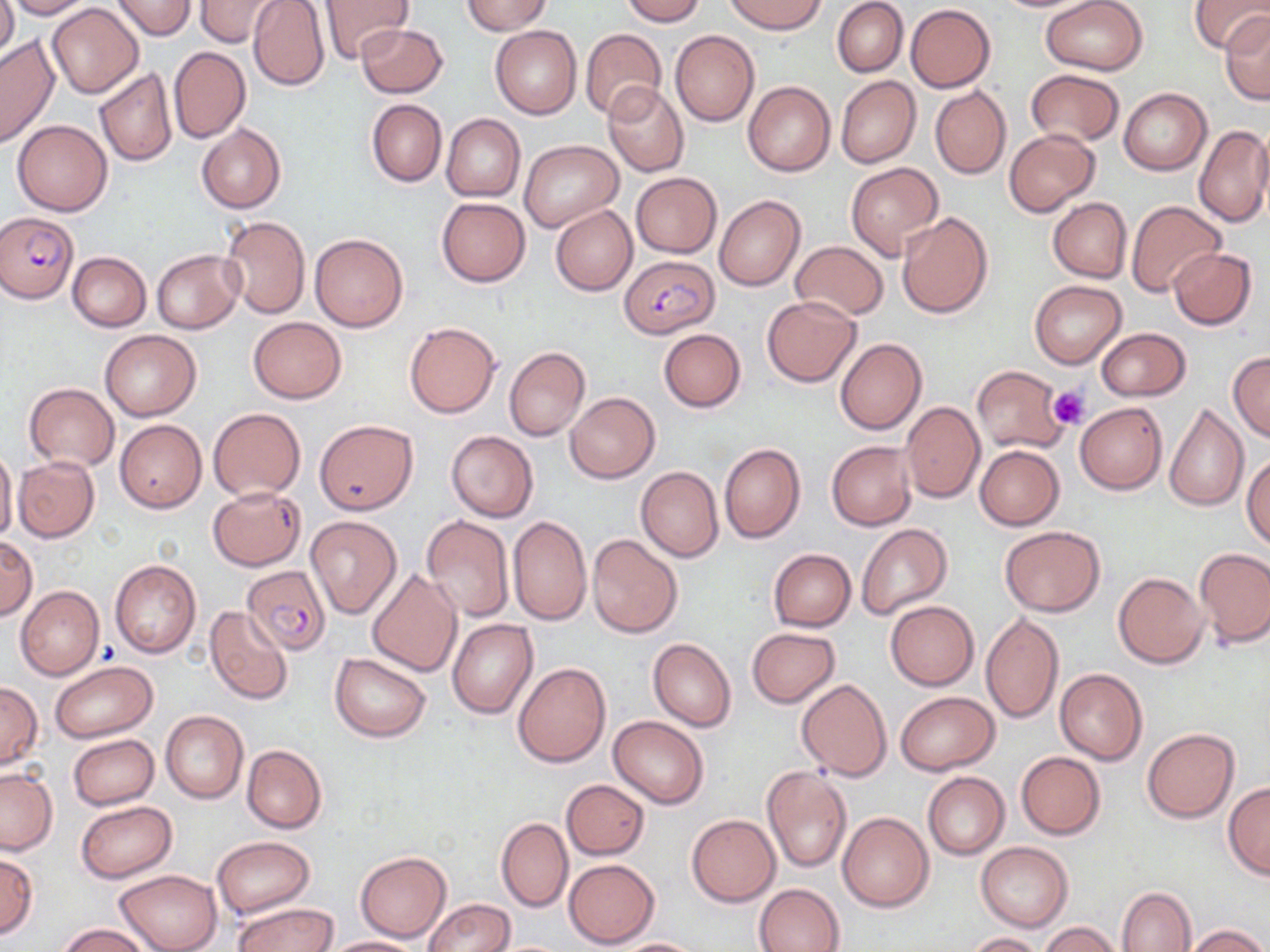

Summary:
  - Coordinate format: approximate bounding boxes as named x1/y1/x2/y2 corners in pixels
  - Plasmodium falciparum-infected red blood cell locations: (x1=0, y1=214, x2=78, y2=303), (x1=619, y1=255, x2=718, y2=338), (x1=242, y1=564, x2=331, y2=655)
  - Platelet locations: (x1=1048, y1=386, x2=1090, y2=430)
  - Uninfected red blood cell locations: (x1=0, y1=0, x2=17, y2=64), (x1=5, y1=0, x2=95, y2=19), (x1=111, y1=0, x2=196, y2=40), (x1=195, y1=0, x2=284, y2=48), (x1=317, y1=0, x2=413, y2=63), (x1=465, y1=0, x2=550, y2=35), (x1=620, y1=0, x2=705, y2=25), (x1=724, y1=0, x2=826, y2=34), (x1=832, y1=0, x2=908, y2=77), (x1=1042, y1=0, x2=1147, y2=75), (x1=1189, y1=0, x2=1268, y2=53), (x1=249, y1=1, x2=331, y2=92), (x1=46, y1=3, x2=144, y2=98), (x1=906, y1=4, x2=996, y2=92), (x1=1219, y1=12, x2=1270, y2=105), (x1=356, y1=23, x2=448, y2=98), (x1=490, y1=25, x2=582, y2=119), (x1=580, y1=28, x2=666, y2=121), (x1=670, y1=30, x2=759, y2=126), (x1=0, y1=34, x2=59, y2=147), (x1=170, y1=46, x2=250, y2=143), (x1=94, y1=69, x2=178, y2=166), (x1=1027, y1=69, x2=1123, y2=146), (x1=835, y1=76, x2=921, y2=169), (x1=743, y1=81, x2=835, y2=177), (x1=603, y1=83, x2=689, y2=176), (x1=930, y1=85, x2=1011, y2=179), (x1=1120, y1=87, x2=1212, y2=176), (x1=367, y1=99, x2=447, y2=188), (x1=441, y1=114, x2=525, y2=202), (x1=12, y1=120, x2=112, y2=216), (x1=197, y1=124, x2=286, y2=214), (x1=1195, y1=125, x2=1270, y2=228), (x1=1253, y1=128, x2=1270, y2=219), (x1=1004, y1=129, x2=1099, y2=217), (x1=519, y1=140, x2=623, y2=232), (x1=844, y1=162, x2=944, y2=261), (x1=629, y1=172, x2=722, y2=258), (x1=714, y1=195, x2=806, y2=291), (x1=437, y1=197, x2=531, y2=286), (x1=1048, y1=197, x2=1132, y2=283), (x1=1126, y1=201, x2=1226, y2=298), (x1=551, y1=204, x2=637, y2=296), (x1=897, y1=212, x2=994, y2=318), (x1=219, y1=216, x2=310, y2=318), (x1=308, y1=233, x2=408, y2=332), (x1=789, y1=242, x2=888, y2=321), (x1=1168, y1=248, x2=1256, y2=330), (x1=152, y1=249, x2=243, y2=333), (x1=67, y1=251, x2=151, y2=331), (x1=1028, y1=278, x2=1127, y2=368), (x1=762, y1=296, x2=861, y2=387), (x1=249, y1=317, x2=346, y2=404), (x1=403, y1=321, x2=501, y2=418), (x1=1097, y1=327, x2=1189, y2=401), (x1=659, y1=329, x2=746, y2=412), (x1=100, y1=330, x2=201, y2=420), (x1=834, y1=336, x2=928, y2=435), (x1=504, y1=346, x2=590, y2=441), (x1=1229, y1=352, x2=1270, y2=442), (x1=971, y1=365, x2=1068, y2=453), (x1=24, y1=382, x2=118, y2=470), (x1=564, y1=392, x2=660, y2=483), (x1=901, y1=401, x2=985, y2=502), (x1=1074, y1=401, x2=1168, y2=495), (x1=1165, y1=403, x2=1249, y2=512), (x1=209, y1=407, x2=305, y2=502), (x1=115, y1=419, x2=206, y2=513), (x1=314, y1=419, x2=417, y2=514), (x1=446, y1=431, x2=538, y2=521), (x1=827, y1=441, x2=917, y2=531), (x1=719, y1=443, x2=805, y2=543), (x1=975, y1=445, x2=1064, y2=530), (x1=0, y1=448, x2=19, y2=545), (x1=1242, y1=453, x2=1270, y2=549), (x1=13, y1=455, x2=100, y2=541), (x1=636, y1=466, x2=723, y2=562), (x1=209, y1=487, x2=304, y2=570), (x1=421, y1=515, x2=514, y2=621), (x1=508, y1=515, x2=592, y2=625), (x1=305, y1=516, x2=402, y2=618), (x1=855, y1=524, x2=953, y2=619), (x1=999, y1=525, x2=1105, y2=617), (x1=0, y1=535, x2=38, y2=621), (x1=587, y1=535, x2=682, y2=638), (x1=1195, y1=547, x2=1270, y2=647), (x1=768, y1=548, x2=855, y2=632), (x1=110, y1=558, x2=201, y2=659), (x1=367, y1=568, x2=463, y2=677), (x1=1113, y1=572, x2=1208, y2=668), (x1=16, y1=586, x2=104, y2=679), (x1=885, y1=600, x2=979, y2=690), (x1=205, y1=606, x2=293, y2=705), (x1=979, y1=612, x2=1064, y2=726), (x1=448, y1=619, x2=538, y2=718), (x1=747, y1=627, x2=840, y2=707), (x1=478, y1=632, x2=581, y2=751), (x1=648, y1=638, x2=737, y2=732), (x1=330, y1=652, x2=431, y2=741), (x1=49, y1=660, x2=159, y2=742), (x1=514, y1=661, x2=611, y2=769), (x1=1054, y1=668, x2=1148, y2=765), (x1=797, y1=679, x2=892, y2=781), (x1=0, y1=681, x2=42, y2=769), (x1=894, y1=691, x2=1000, y2=775), (x1=161, y1=710, x2=249, y2=803), (x1=608, y1=716, x2=708, y2=808), (x1=1142, y1=727, x2=1240, y2=822), (x1=68, y1=734, x2=158, y2=810), (x1=242, y1=744, x2=327, y2=834), (x1=1016, y1=752, x2=1105, y2=839), (x1=762, y1=766, x2=851, y2=873), (x1=0, y1=767, x2=58, y2=856), (x1=922, y1=772, x2=1009, y2=859), (x1=561, y1=779, x2=650, y2=860), (x1=1222, y1=782, x2=1270, y2=879), (x1=76, y1=800, x2=177, y2=882), (x1=837, y1=811, x2=935, y2=912), (x1=687, y1=814, x2=780, y2=907), (x1=496, y1=817, x2=573, y2=912), (x1=212, y1=836, x2=314, y2=918), (x1=975, y1=841, x2=1073, y2=931), (x1=355, y1=851, x2=451, y2=943), (x1=0, y1=852, x2=38, y2=939), (x1=563, y1=858, x2=660, y2=948), (x1=114, y1=869, x2=220, y2=952), (x1=754, y1=883, x2=844, y2=951), (x1=1117, y1=887, x2=1196, y2=952), (x1=424, y1=899, x2=515, y2=952), (x1=232, y1=902, x2=336, y2=952), (x1=1039, y1=922, x2=1123, y2=952), (x1=58, y1=924, x2=153, y2=952), (x1=1183, y1=925, x2=1267, y2=952), (x1=966, y1=932, x2=1043, y2=952), (x1=322, y1=936, x2=422, y2=952), (x1=610, y1=937, x2=709, y2=951)
  - Slide-level diagnosis: Plasmodium falciparum
  - Magnification: 1000x
  - Field of view: single
  - Modality: optical microscopy
  - Preparation: thin blood smear
  - Stain: May-Grünwald-Giemsa
  - Image size: 1270×952 pixels